Assess the morphology of the red blood cells.
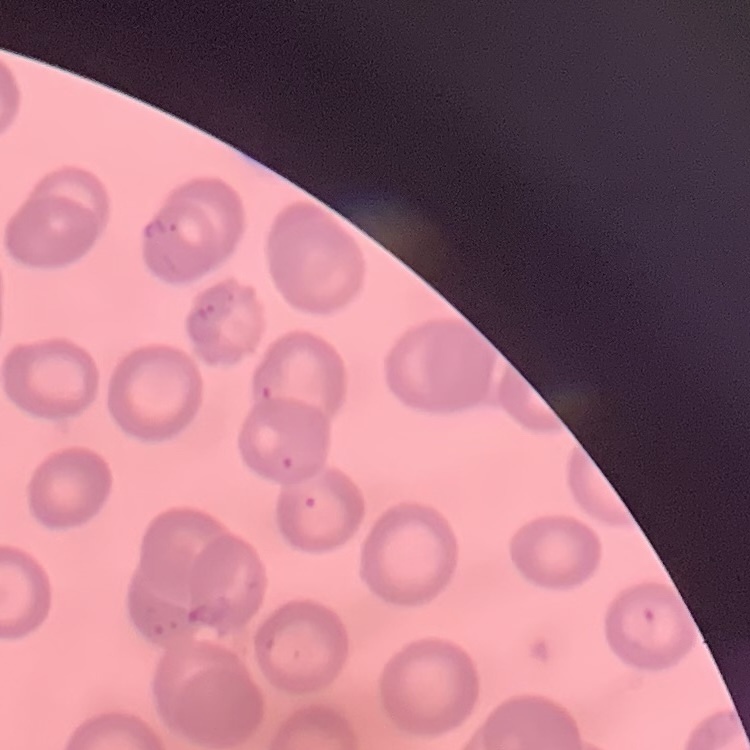
No rouleaux formation.

One tile cut from a larger photomicrograph. Thin peripheral smear. Stained with either Field's or Giemsa.